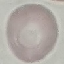

result = negative for malaria parasites
image type = cell patch, automatically extracted from a larger field of view and resized to 64 × 64 pixels
stain = Giemsa
capture = smartphone through the microscope eyepiece
preparation = thin blood smear